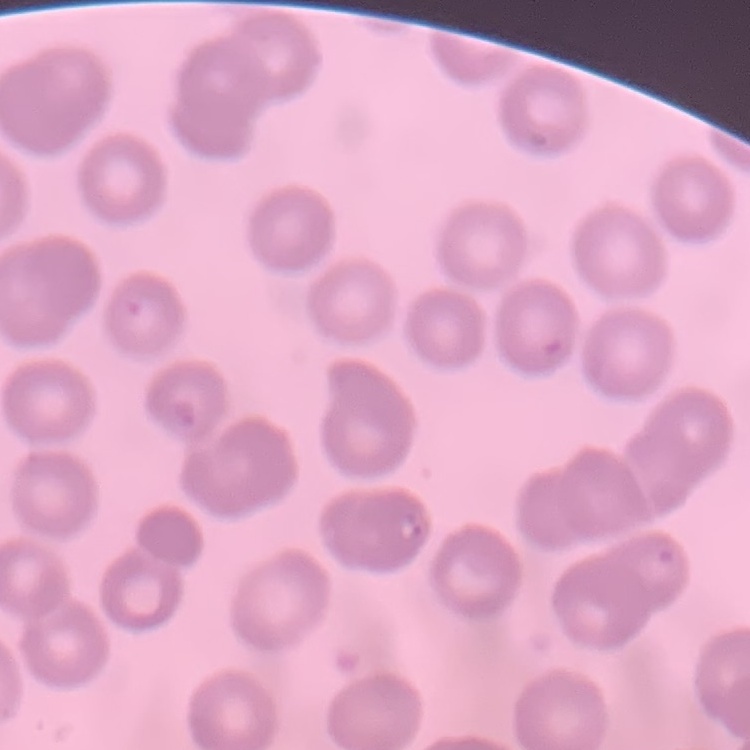
Summary:
  - Erythrocyte morphology: no rouleaux formation
  - Preparation: thin blood smear
  - Image type: square crop of a larger photomicrograph
  - Stain: Field's or Giemsa